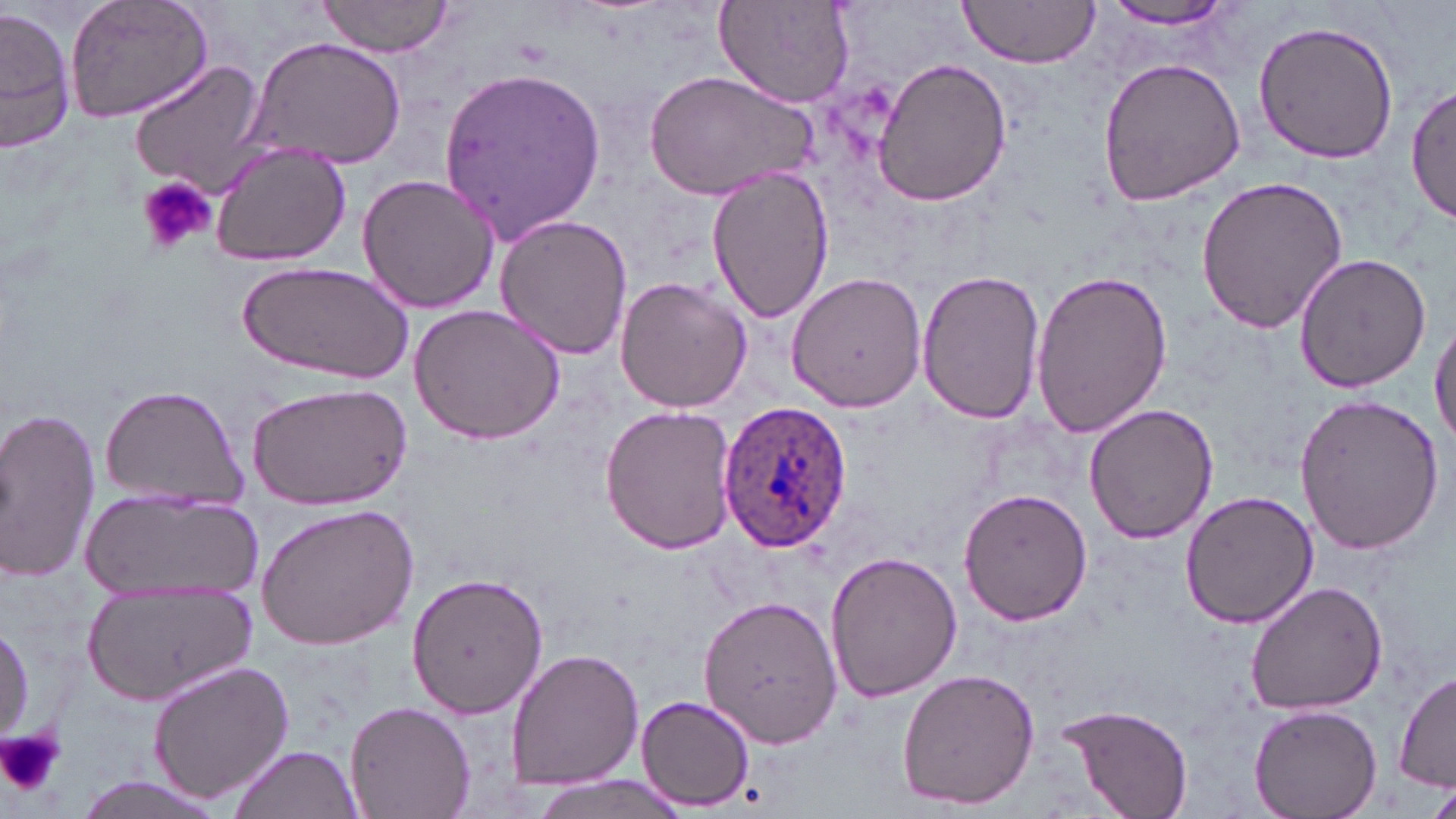
slide-level diagnosis = Plasmodium ovale
image size = 1456×819 pixels
modality = optical microscopy
field of view = one of a larger specimen
preparation = thin blood smear
Plasmodium ovale-infected red blood cell locations = approximate bounding boxes as [x1, y1, x2, y2] in pixels: [719, 402, 853, 553]
magnification = 1000x
uninfected red blood cell locations = approximate bounding boxes as [x1, y1, x2, y2] in pixels: [63, 0, 215, 125], [314, 0, 455, 58], [957, 0, 1102, 68], [1094, 0, 1242, 30], [714, 2, 858, 109], [0, 9, 75, 155], [1251, 20, 1400, 165], [246, 37, 408, 172], [1097, 56, 1246, 206], [873, 57, 1009, 206], [128, 59, 266, 193], [438, 63, 606, 240], [643, 70, 814, 200], [1407, 78, 1456, 224], [208, 141, 350, 267], [708, 168, 835, 324], [357, 171, 500, 313], [1194, 175, 1354, 336], [493, 214, 633, 363], [1292, 252, 1431, 394], [239, 261, 413, 383], [916, 268, 1042, 422], [1029, 269, 1173, 440], [785, 272, 928, 412], [614, 277, 752, 414], [410, 304, 567, 445], [1431, 315, 1456, 450], [244, 382, 413, 510], [98, 384, 251, 509], [1295, 394, 1444, 555], [1085, 403, 1219, 544], [599, 405, 738, 554], [0, 406, 102, 585], [959, 487, 1093, 626], [1178, 489, 1318, 629], [83, 490, 258, 603], [257, 503, 420, 650], [827, 551, 962, 704], [406, 570, 549, 718], [1245, 581, 1389, 718], [85, 585, 259, 704], [700, 594, 844, 749], [506, 648, 643, 788], [147, 660, 294, 803], [896, 668, 1040, 810], [1396, 669, 1455, 793], [635, 695, 754, 811], [344, 701, 476, 819], [1058, 702, 1193, 819], [1248, 705, 1380, 818], [228, 745, 364, 819], [524, 775, 686, 819], [71, 776, 234, 818], [1424, 779, 1456, 819]
platelet locations = approximate bounding boxes as [x1, y1, x2, y2] in pixels: [134, 174, 219, 257], [0, 728, 63, 797]
stain = May-Grünwald-Giemsa